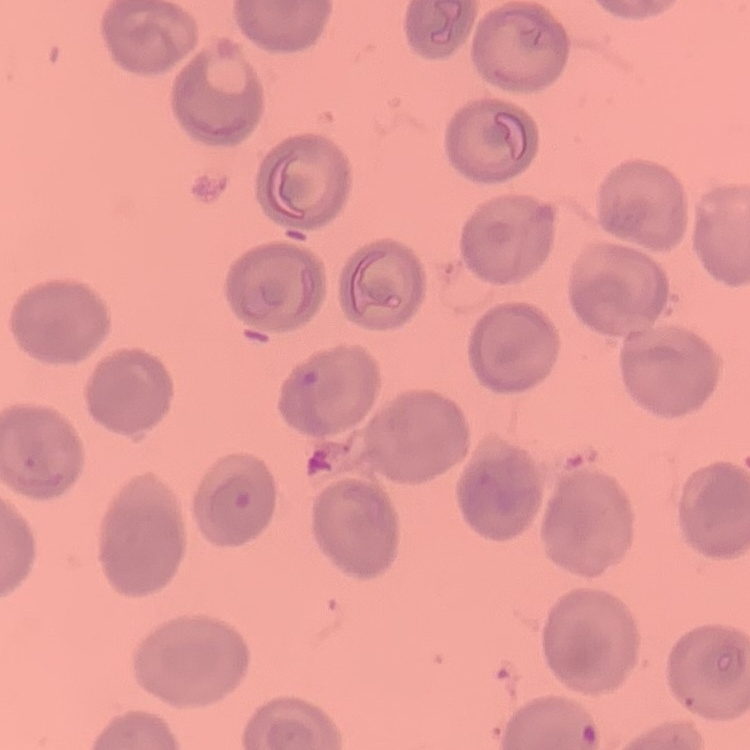
The red blood cells show no rouleaux formation. Stained with either Field's or Giemsa. Thin blood smear. One tile cut from a larger photomicrograph.